State the preparation type.
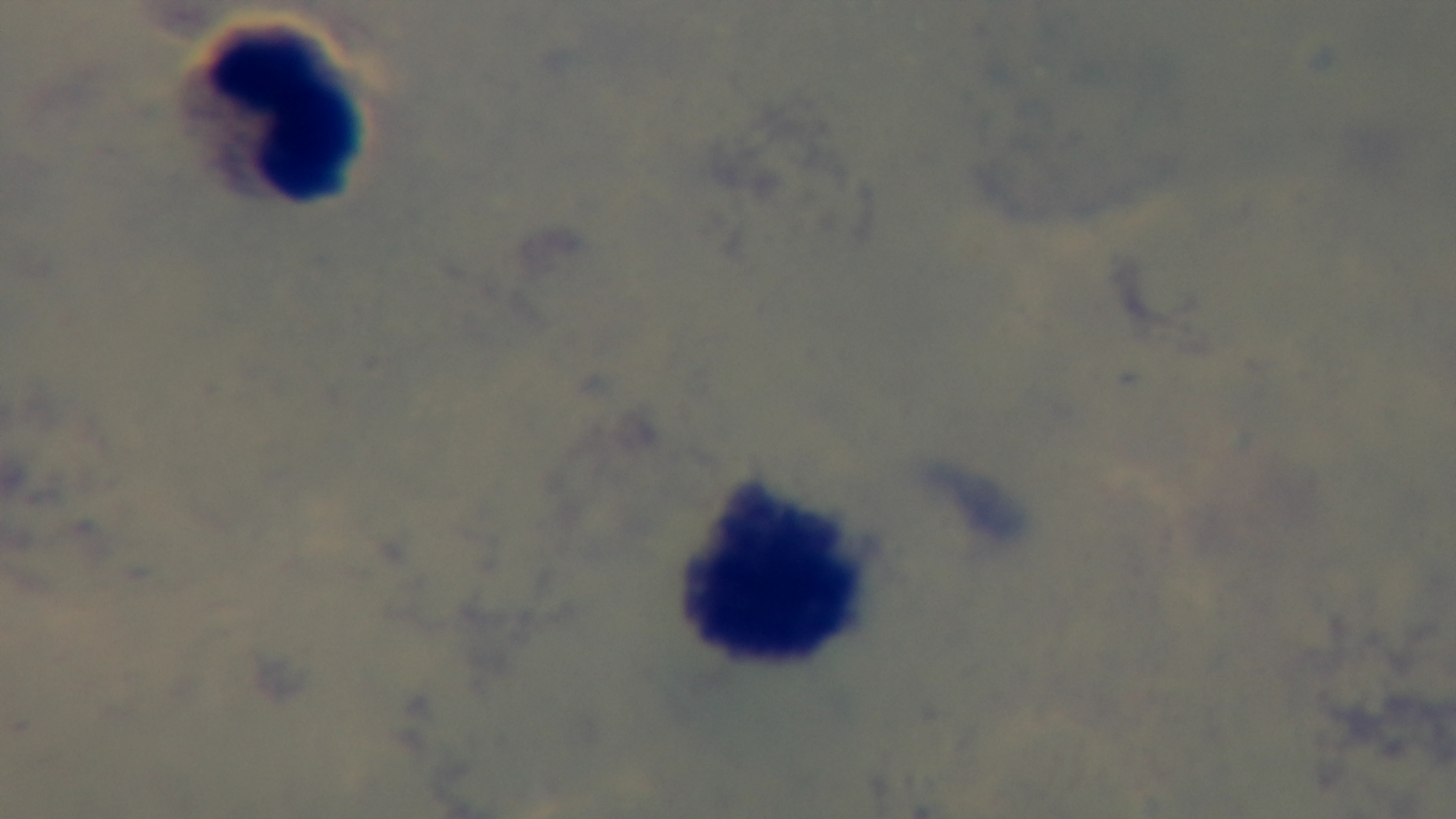

Thick.

Summary:
  - Malaria status: negative
  - Capture: mounted 4K digital camera
  - Field of view: single
  - Objective: 100x oil immersion
  - Stain: Giemsa
  - Modality: light microscopy